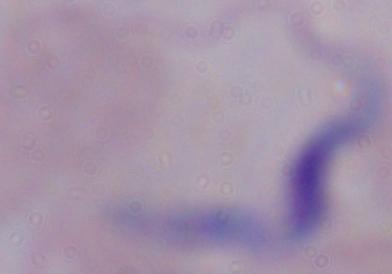

Micrograph. Captured at 1000x magnification. A trypanosome is shown.